Describe the morphology of the red blood cells.
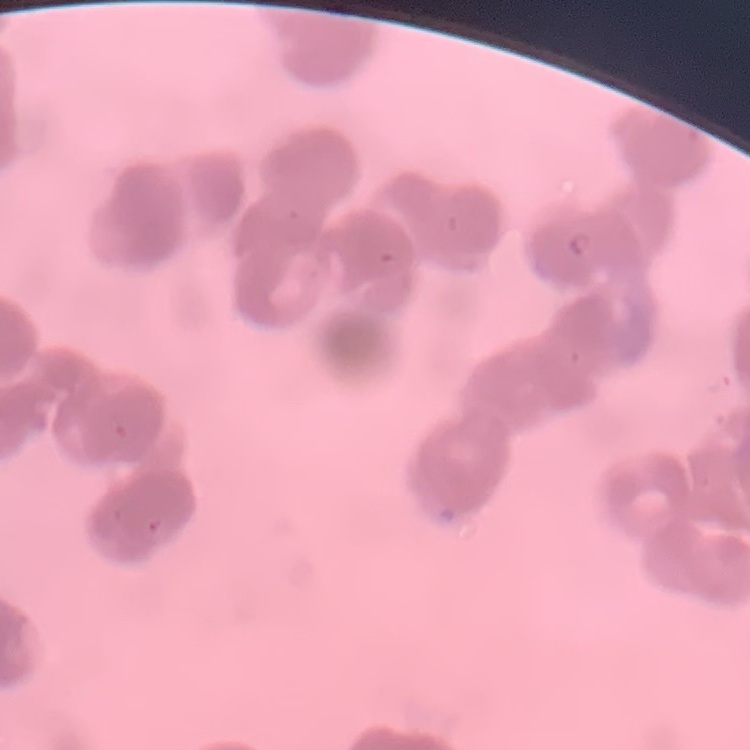
They show rouleaux formation.

Summary:
  - Image type: one tile cut from a larger photomicrograph
  - Preparation: thin blood film
  - Stain: Field's or Giemsa